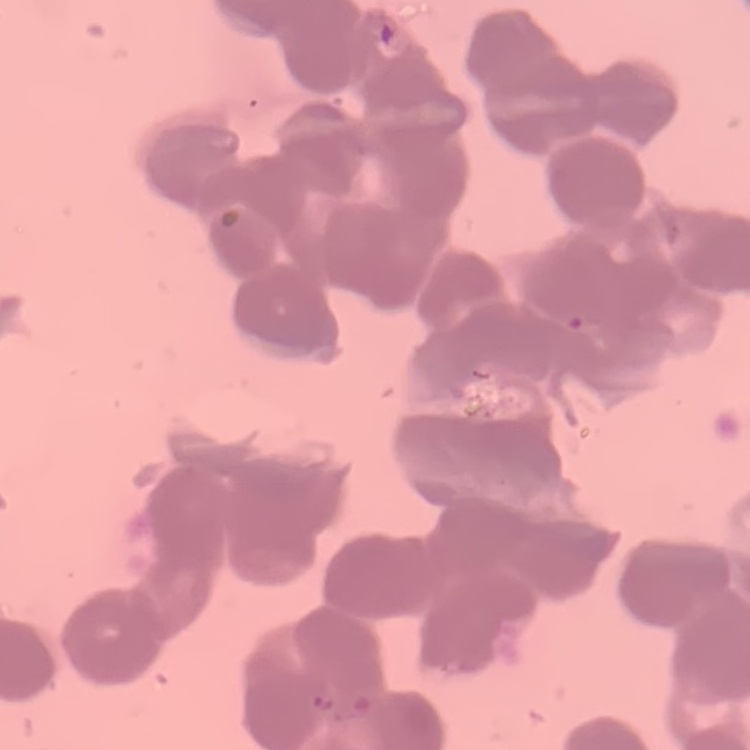
Summary:
  - Red blood cell morphology: rouleaux formation
  - Image type: square crop of a larger photomicrograph
  - Preparation: thin blood smear
  - Stain: Field's or Giemsa